State which parasite is depicted.
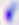
Toxoplasma gondii.

magnification = 400x
modality = photomicrograph